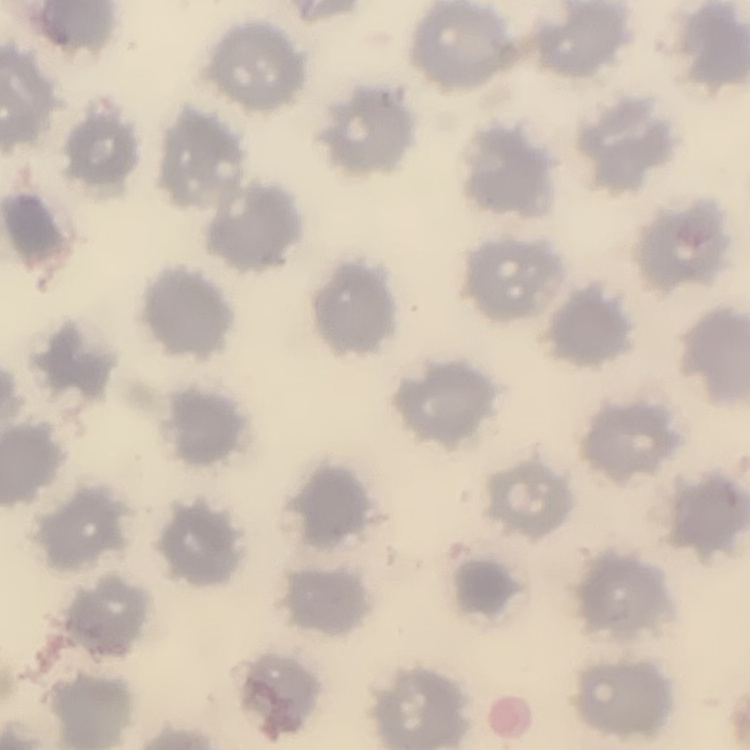
red blood cell morphology = no rouleaux formation
image type = one tile cut from a larger photomicrograph
preparation = thin blood film
stain = Field's or Giemsa